Name the parasite shown.
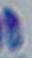
Toxoplasma gondii.

Captured at 1000x magnification. Photomicrograph.